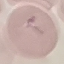
Summary:
  - Result: negative for malaria parasites
  - Preparation: thin smear
  - Image type: automatically extracted cell patch, resized to 64 × 64 pixels
  - Stain: Giemsa
  - Capture: smartphone camera at the microscope eyepiece